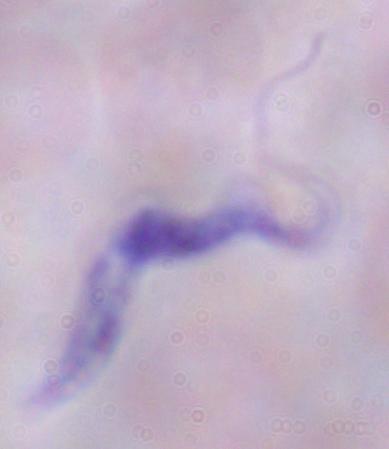
Summary:
  - Identification: trypanosome
  - Modality: micrograph
  - Magnification: 1000x